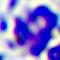
Summary:
  - Modality: photomicrograph
  - Identification: white blood cell
  - Magnification: 400x